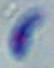
Summary:
  - Magnification: 1000x
  - Modality: micrograph
  - Identification: Toxoplasma gondii